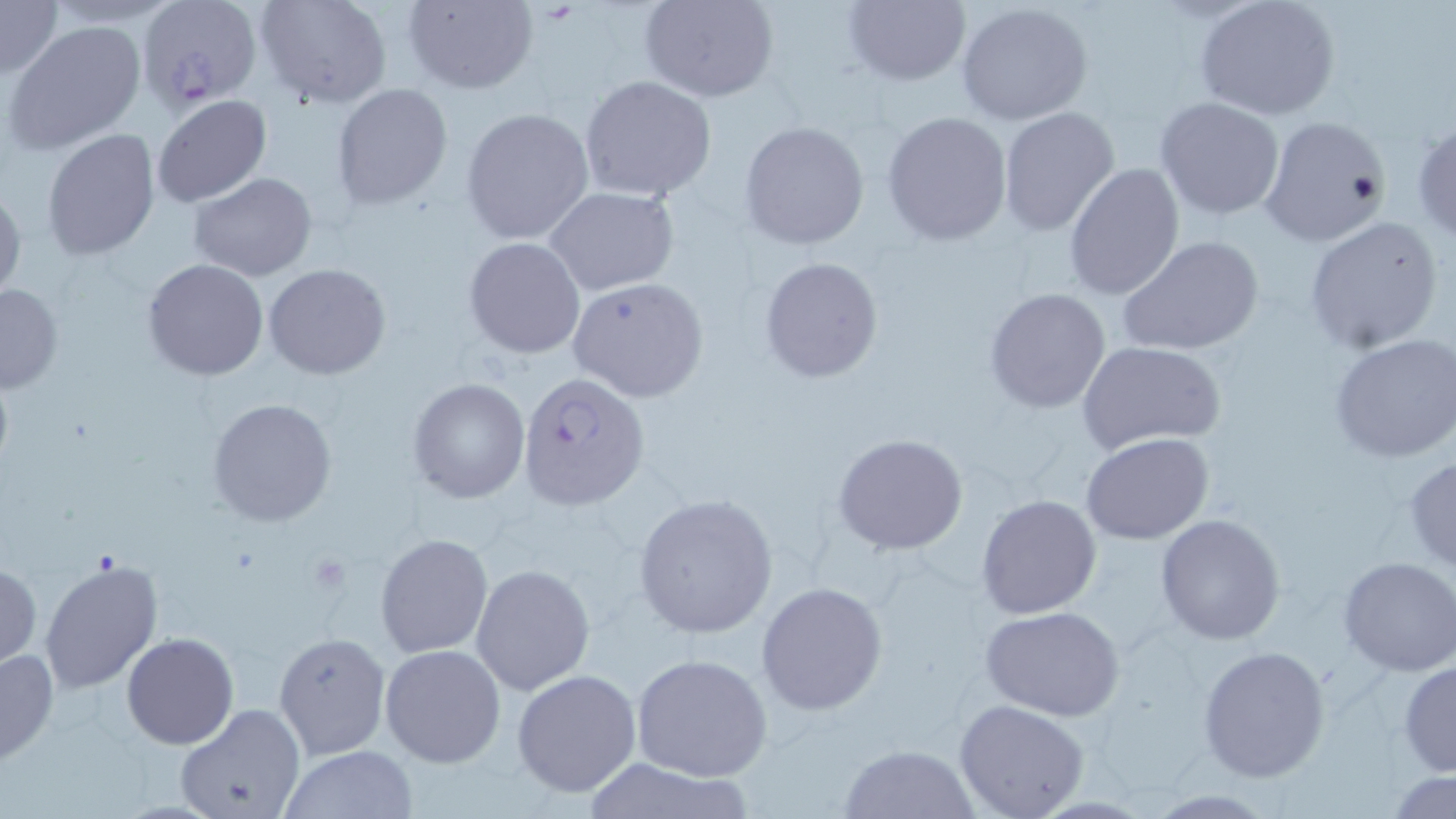

Summary:
  - Coordinate format: approximate bounding boxes as [x1, y1, x2, y2] in pixels
  - Uninfected red blood cell locations: [0, 0, 62, 81], [44, 0, 186, 26], [254, 0, 392, 109], [402, 0, 537, 95], [641, 0, 779, 103], [842, 0, 969, 86], [1195, 0, 1340, 121], [954, 3, 1095, 127], [6, 19, 146, 154], [578, 76, 718, 203], [330, 85, 452, 209], [152, 95, 272, 207], [1155, 96, 1285, 219], [460, 106, 595, 245], [998, 107, 1121, 236], [882, 111, 1013, 246], [1257, 114, 1390, 248], [1411, 117, 1456, 242], [739, 120, 870, 251], [43, 130, 161, 261], [1062, 163, 1185, 303], [187, 172, 317, 281], [0, 184, 25, 304], [544, 186, 678, 296], [1302, 215, 1443, 355], [1118, 235, 1264, 356], [463, 238, 585, 358], [758, 256, 885, 384], [142, 258, 269, 382], [264, 264, 391, 380], [568, 277, 709, 402], [0, 283, 62, 394], [984, 288, 1111, 413], [1329, 333, 1456, 463], [1079, 341, 1224, 453], [407, 378, 530, 504], [207, 397, 338, 527], [1082, 431, 1214, 544], [832, 432, 968, 555], [1404, 455, 1456, 572], [1096, 457, 1247, 610], [631, 492, 779, 640], [976, 494, 1102, 618], [1156, 514, 1287, 645], [375, 532, 494, 658], [1337, 557, 1456, 676], [40, 558, 164, 696], [0, 559, 41, 671], [471, 564, 594, 695], [755, 581, 888, 716], [978, 605, 1125, 720], [273, 631, 391, 759], [120, 632, 238, 749], [379, 643, 507, 769], [1197, 644, 1330, 781], [0, 648, 58, 766], [631, 652, 772, 781], [1398, 660, 1456, 777], [512, 668, 642, 798], [953, 699, 1089, 819], [174, 704, 307, 819], [839, 742, 979, 818], [280, 746, 417, 818], [578, 756, 754, 819], [1386, 771, 1456, 817]
  - Plasmodium falciparum-infected red blood cell locations: [138, 1, 262, 112], [516, 372, 647, 512]
  - Slide-level diagnosis: Plasmodium falciparum
  - Field of view: single
  - Stain: May-Grünwald-Giemsa
  - Magnification: 1000x
  - Modality: optical microscopy
  - Preparation: thin blood film
  - Image size: 1456×819 pixels